Report the malaria status of this cell.
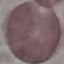

It is uninfected.

capture = smartphone camera at the microscope eyepiece
preparation = thin blood smear
image type = automatically extracted cell patch, resized to 64 × 64 pixels
stain = Giemsa